Name the parasite shown.
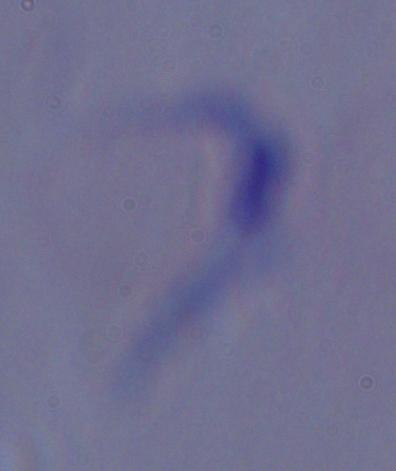
This is a trypanosome.

magnification = 1000x
modality = photomicrograph